Give the extent of all uninfected red blood cells.
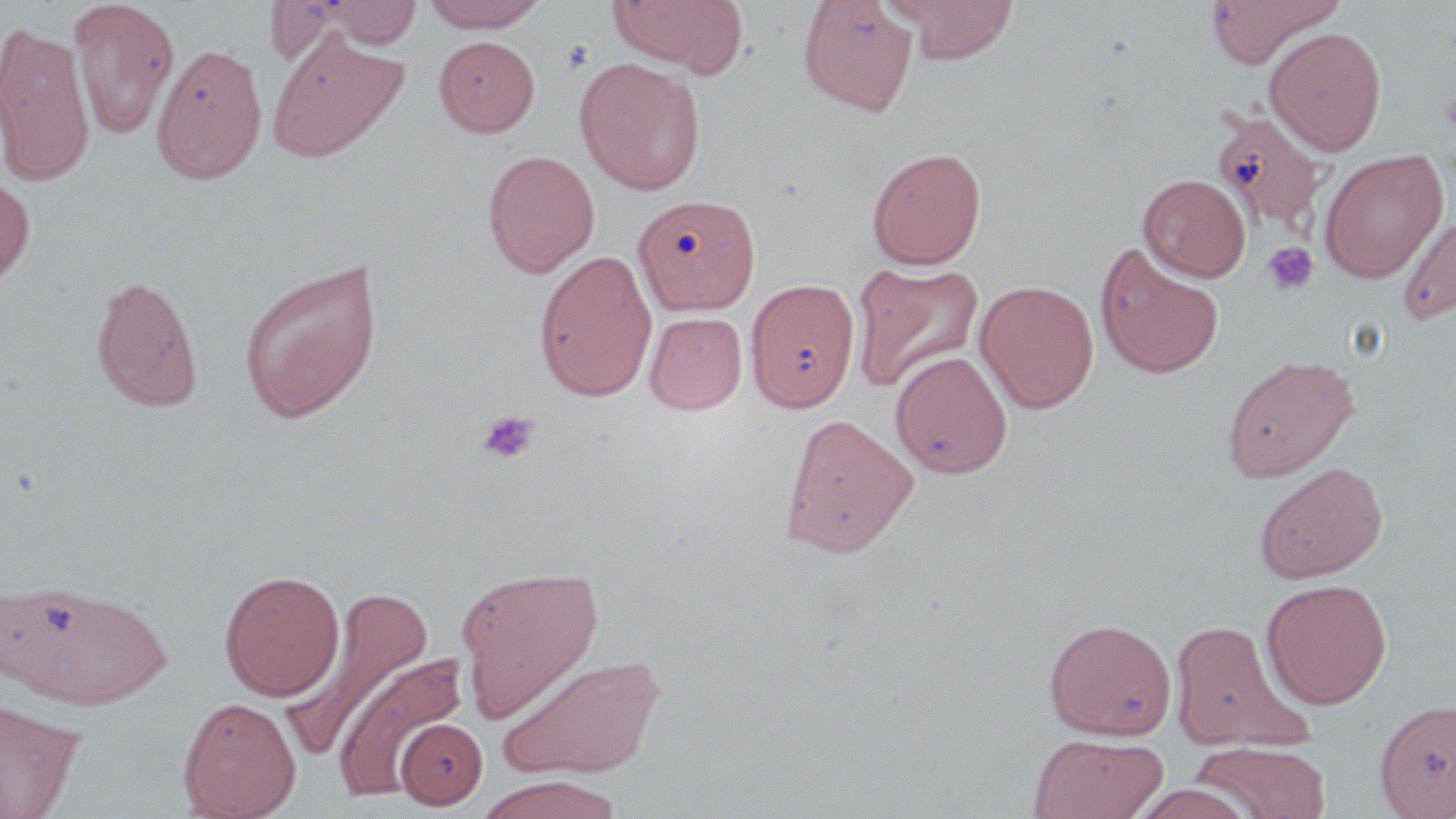

Approximate bounding boxes as named x1/y1/x2/y2 corners in pixels.
Uninfected red blood cells: (x1=68, y1=0, x2=179, y2=140), (x1=319, y1=0, x2=423, y2=49), (x1=420, y1=0, x2=548, y2=32), (x1=607, y1=0, x2=747, y2=75), (x1=886, y1=0, x2=1020, y2=64), (x1=1205, y1=0, x2=1344, y2=68), (x1=263, y1=1, x2=404, y2=67), (x1=798, y1=1, x2=919, y2=116), (x1=0, y1=19, x2=95, y2=187), (x1=1264, y1=26, x2=1387, y2=155), (x1=267, y1=30, x2=410, y2=163), (x1=433, y1=35, x2=540, y2=137), (x1=152, y1=41, x2=267, y2=185), (x1=574, y1=57, x2=706, y2=195), (x1=1214, y1=110, x2=1329, y2=235), (x1=866, y1=147, x2=987, y2=269), (x1=1319, y1=149, x2=1449, y2=282), (x1=482, y1=150, x2=599, y2=277), (x1=0, y1=171, x2=35, y2=291), (x1=1140, y1=177, x2=1252, y2=285), (x1=634, y1=193, x2=761, y2=314), (x1=1397, y1=210, x2=1456, y2=324), (x1=1095, y1=243, x2=1224, y2=380), (x1=534, y1=249, x2=658, y2=402), (x1=238, y1=258, x2=384, y2=424), (x1=850, y1=260, x2=984, y2=393), (x1=89, y1=274, x2=204, y2=412), (x1=745, y1=278, x2=861, y2=412), (x1=976, y1=280, x2=1099, y2=414), (x1=645, y1=311, x2=747, y2=415), (x1=890, y1=351, x2=1013, y2=479), (x1=1221, y1=354, x2=1360, y2=482), (x1=779, y1=411, x2=918, y2=558), (x1=1254, y1=462, x2=1388, y2=583), (x1=456, y1=564, x2=604, y2=723), (x1=220, y1=569, x2=345, y2=700), (x1=1, y1=577, x2=172, y2=709), (x1=1261, y1=578, x2=1393, y2=709), (x1=288, y1=582, x2=438, y2=755), (x1=1044, y1=617, x2=1177, y2=740), (x1=1169, y1=618, x2=1303, y2=750), (x1=334, y1=651, x2=470, y2=799), (x1=497, y1=652, x2=665, y2=780), (x1=178, y1=697, x2=302, y2=819), (x1=0, y1=698, x2=83, y2=819), (x1=1374, y1=698, x2=1456, y2=818), (x1=396, y1=718, x2=487, y2=810), (x1=1028, y1=733, x2=1169, y2=819), (x1=1191, y1=741, x2=1330, y2=818), (x1=475, y1=774, x2=624, y2=819), (x1=1129, y1=782, x2=1259, y2=818).

Platelet locations: (x1=562, y1=40, x2=594, y2=75), (x1=1440, y1=84, x2=1456, y2=143), (x1=1263, y1=242, x2=1319, y2=295), (x1=478, y1=410, x2=540, y2=464). Slide-level diagnosis: no evidence of blood parasites. May-Grünwald-Giemsa stain. Image is 1456×819 pixels. Captured at 1000x magnification. Thin blood film. Light microscopy. Single field of view.